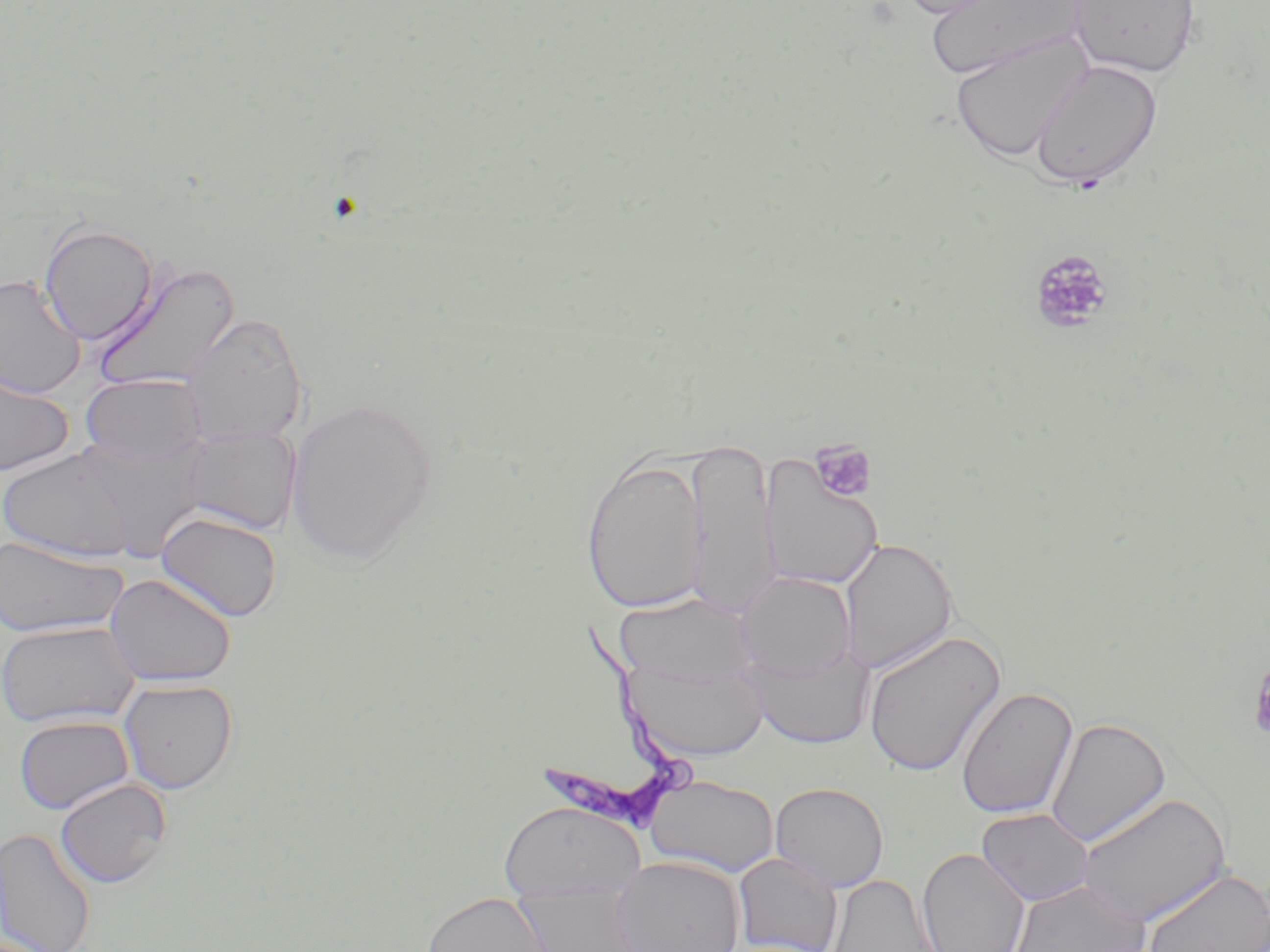

Summary:
  - Coordinate format: approximate bounding boxes as (x1,y1)-(x2,y2) corner pairs in pixels
  - Trypanosoma brucei locations: (532,617)-(699,838)
  - Platelet locations: (1028,249)-(1116,335), (809,439)-(877,504), (1247,653)-(1270,743)
  - Uninfected red blood cell locations: (894,0)-(1013,18), (923,0)-(1083,81), (1068,0)-(1202,79), (948,30)-(1095,163), (1029,59)-(1163,189), (38,222)-(158,345), (91,257)-(242,395), (0,274)-(86,398), (181,312)-(308,447), (0,369)-(75,477), (80,374)-(206,468), (285,396)-(439,567), (182,426)-(301,535), (53,435)-(212,562), (685,437)-(778,617), (0,445)-(146,563), (579,451)-(710,616), (758,452)-(885,590), (154,511)-(282,622), (0,535)-(129,638), (838,538)-(958,674), (735,571)-(857,683), (104,573)-(237,687), (614,592)-(758,694), (0,621)-(140,728), (863,629)-(1006,778), (742,637)-(876,751), (622,653)-(770,763), (118,678)-(238,794), (956,686)-(1078,821), (13,715)-(134,815), (1045,716)-(1172,847), (643,774)-(780,878), (54,778)-(173,888), (769,781)-(889,892), (1075,791)-(1232,928), (497,801)-(645,904), (976,808)-(1094,906), (0,827)-(97,952), (917,846)-(1030,952), (733,852)-(844,952), (612,856)-(745,952), (1140,867)-(1270,952), (824,872)-(942,952), (1006,878)-(1151,952), (512,882)-(645,952), (420,891)-(551,952)
  - Slide-level diagnosis: Trypanosoma brucei
  - Magnification: 1000x
  - Field of view: one of a larger specimen
  - Image size: 1270×952 pixels
  - Modality: optical microscopy
  - Stain: May-Grünwald-Giemsa
  - Preparation: thin blood smear